Identify the parasite.
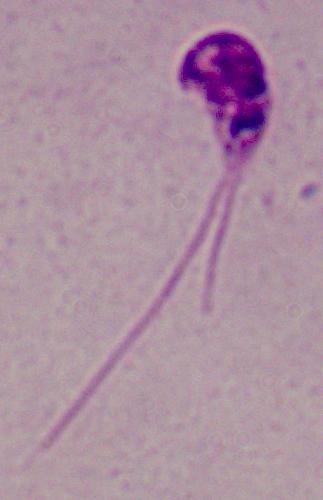
This is Leishmania.

Summary:
  - Modality: micrograph
  - Magnification: 1000x